Give the position of every Plasmodium parasite.
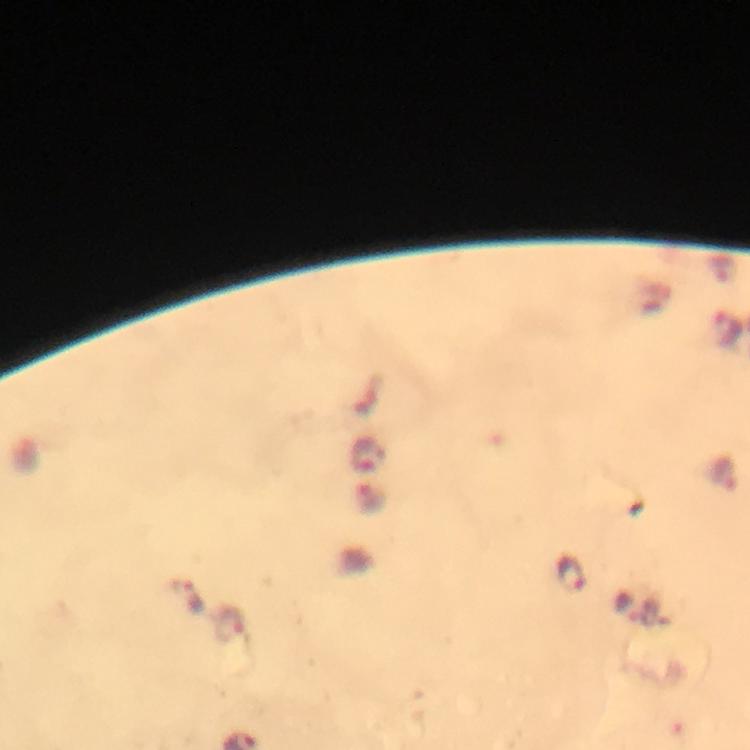

Approximate centers as {x, y} in pixels.
Plasmodium parasites: {367, 456}, {722, 475}, {372, 498}, {573, 573}, {185, 597}, {229, 626}.

{
  "stain": "Giemsa",
  "cropped_from": "one field of view",
  "image_size": "750×750 pixels",
  "context": "from a malaria diagnostic workup",
  "immersion_oil": "used",
  "capture": "smartphone photograph through a microscope",
  "preparation": "thick blood film",
  "magnification": "100x"
}